Locate every uninfected red blood cell.
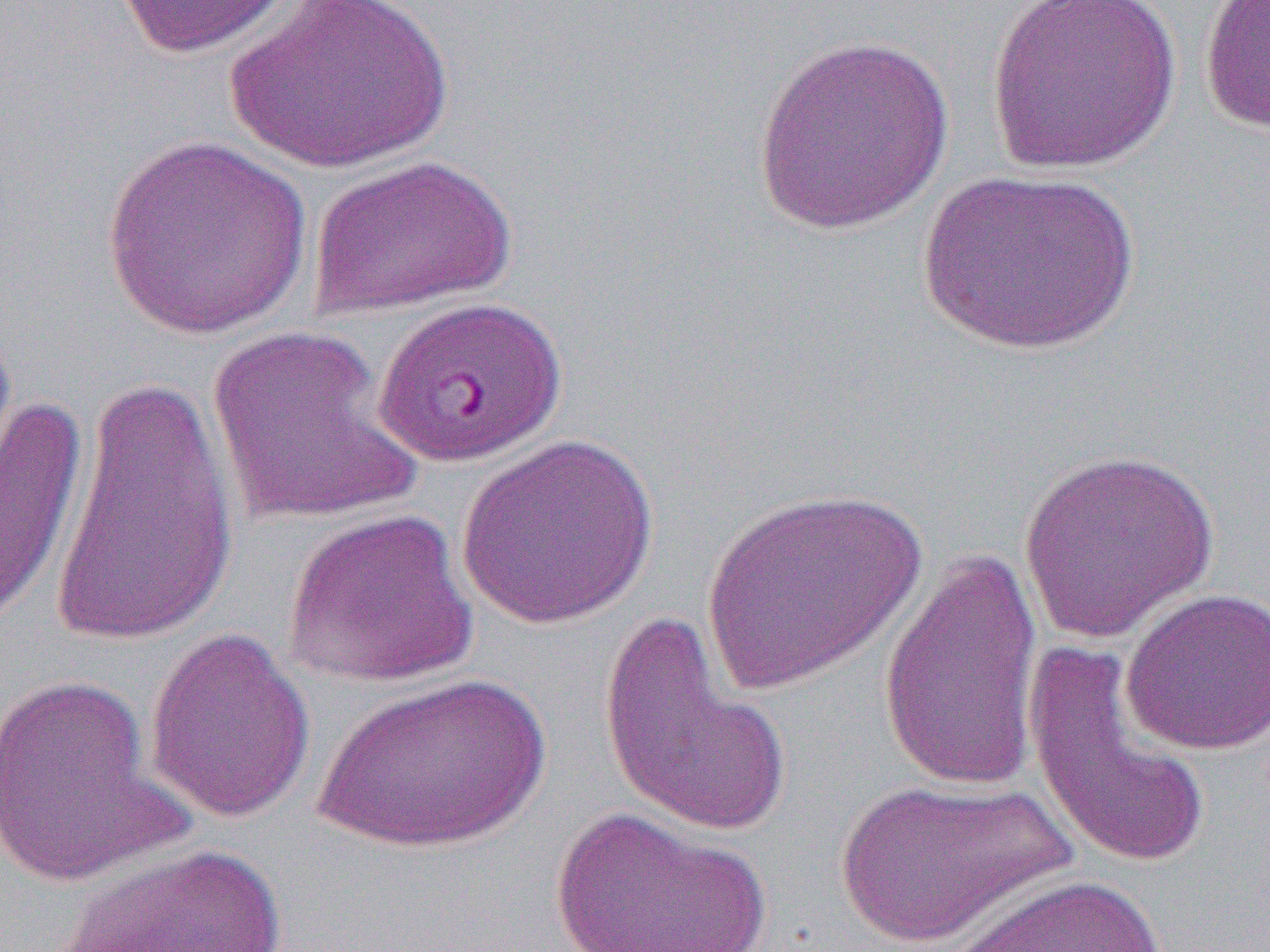
Approximate bounding boxes as named x1/y1/x2/y2 corners in pixels.
Uninfected red blood cells: (x1=111, y1=0, x2=298, y2=59), (x1=224, y1=0, x2=454, y2=174), (x1=986, y1=0, x2=1182, y2=175), (x1=1198, y1=1, x2=1270, y2=134), (x1=751, y1=34, x2=955, y2=237), (x1=101, y1=132, x2=313, y2=341), (x1=307, y1=153, x2=517, y2=320), (x1=917, y1=169, x2=1140, y2=357), (x1=208, y1=326, x2=420, y2=527), (x1=50, y1=368, x2=242, y2=656), (x1=0, y1=396, x2=88, y2=628), (x1=454, y1=435, x2=659, y2=630), (x1=1017, y1=448, x2=1221, y2=643), (x1=701, y1=485, x2=927, y2=696), (x1=282, y1=508, x2=479, y2=689), (x1=878, y1=546, x2=1044, y2=794), (x1=1120, y1=587, x2=1270, y2=756), (x1=597, y1=611, x2=794, y2=838), (x1=144, y1=626, x2=316, y2=824), (x1=1021, y1=645, x2=1215, y2=871), (x1=311, y1=672, x2=552, y2=854), (x1=0, y1=673, x2=189, y2=889), (x1=832, y1=777, x2=1075, y2=948), (x1=547, y1=806, x2=775, y2=952), (x1=59, y1=841, x2=288, y2=952), (x1=944, y1=870, x2=1169, y2=950).

Plasmodium falciparum-infected red blood cell locations: (x1=371, y1=295, x2=567, y2=469). Slide-level diagnosis: Plasmodium falciparum. Image is 1270×952 pixels. Captured at 1000x magnification. Thin blood smear. Single field of view. Light microscopy.